Assess the morphology of the erythrocytes.
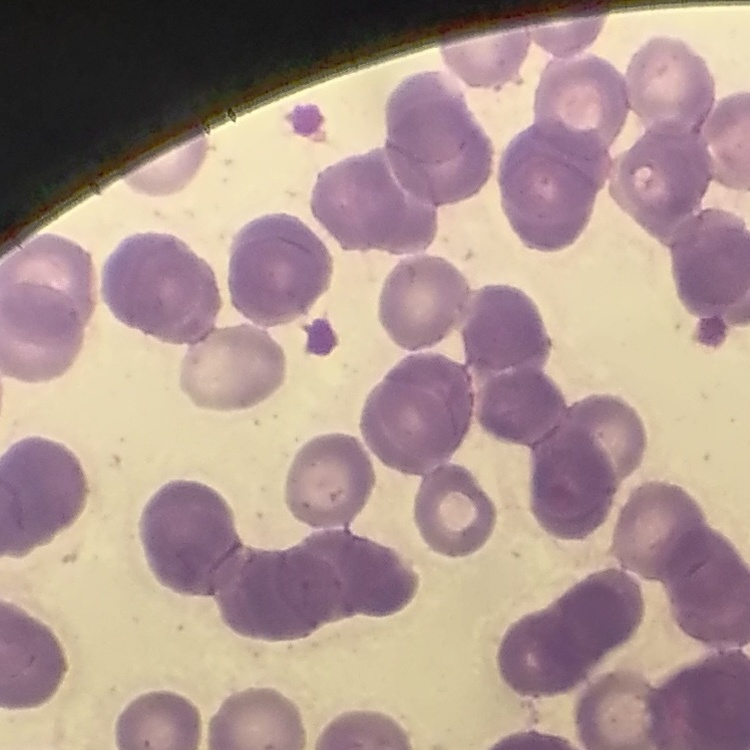
Rouleaux formation.

image type = one tile cut from a larger photomicrograph
stain = Field's or Giemsa
preparation = thin blood film